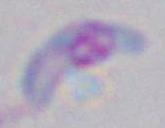

Summary:
  - Modality: micrograph
  - Identification: Toxoplasma gondii
  - Magnification: 1000x